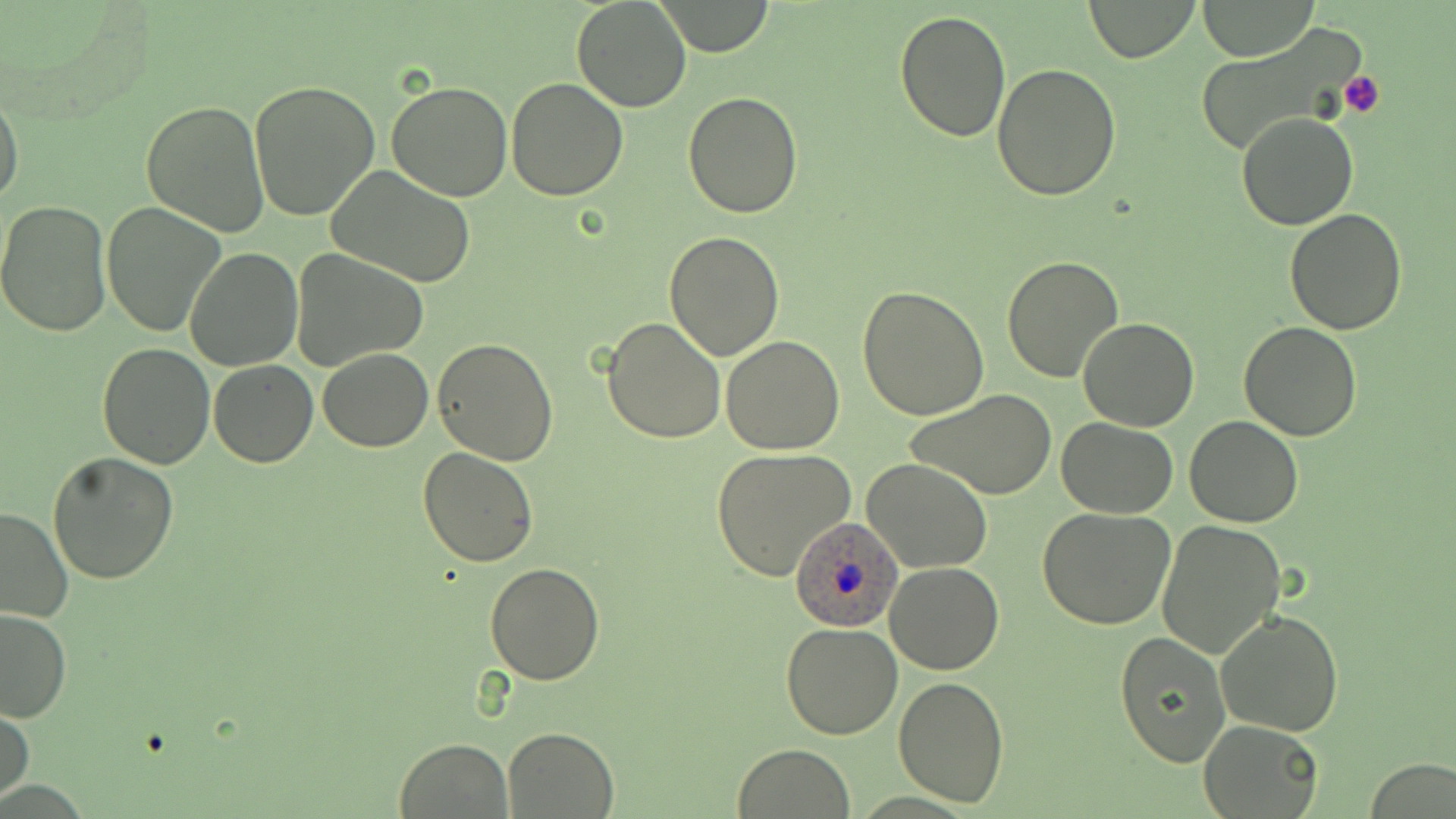
{
  "slide_level_diagnosis": "Plasmodium ovale",
  "stain": "May-Grünwald-Giemsa",
  "image_size": "1456×819 pixels",
  "modality": "optical microscopy",
  "preparation": "thin blood film",
  "plasmodium_ovale_infected_red_blood_cell_locations": "approximate bounding boxes as named x1/y1/x2/y2 corners in pixels: (x1=787, y1=513, x2=906, y2=632)",
  "magnification": "1000x",
  "field_of_view": "one of a larger specimen",
  "uninfected_red_blood_cell_locations": "approximate bounding boxes as named x1/y1/x2/y2 corners in pixels: (x1=571, y1=0, x2=691, y2=112), (x1=1082, y1=0, x2=1201, y2=63), (x1=1198, y1=0, x2=1320, y2=60), (x1=652, y1=1, x2=776, y2=55), (x1=894, y1=8, x2=1011, y2=142), (x1=1186, y1=25, x2=1377, y2=159), (x1=991, y1=62, x2=1122, y2=201), (x1=506, y1=77, x2=630, y2=201), (x1=248, y1=80, x2=380, y2=222), (x1=386, y1=81, x2=514, y2=201), (x1=1, y1=90, x2=25, y2=210), (x1=683, y1=92, x2=803, y2=218), (x1=142, y1=100, x2=269, y2=235), (x1=1236, y1=111, x2=1358, y2=230), (x1=326, y1=165, x2=477, y2=287), (x1=0, y1=199, x2=114, y2=337), (x1=102, y1=201, x2=227, y2=337), (x1=1283, y1=208, x2=1406, y2=334), (x1=663, y1=231, x2=783, y2=361), (x1=185, y1=248, x2=303, y2=370), (x1=292, y1=251, x2=427, y2=369), (x1=1002, y1=255, x2=1125, y2=384), (x1=859, y1=283, x2=990, y2=421), (x1=603, y1=317, x2=727, y2=443), (x1=1078, y1=318, x2=1200, y2=432), (x1=1239, y1=321, x2=1363, y2=441), (x1=721, y1=336, x2=846, y2=455), (x1=432, y1=337, x2=560, y2=464), (x1=97, y1=341, x2=216, y2=468), (x1=318, y1=347, x2=432, y2=451), (x1=208, y1=361, x2=318, y2=468), (x1=905, y1=388, x2=1056, y2=501), (x1=1185, y1=416, x2=1303, y2=528), (x1=1058, y1=419, x2=1179, y2=518), (x1=418, y1=447, x2=539, y2=565), (x1=710, y1=448, x2=857, y2=581), (x1=47, y1=451, x2=180, y2=585), (x1=862, y1=457, x2=993, y2=573), (x1=0, y1=506, x2=74, y2=624), (x1=1036, y1=507, x2=1177, y2=630), (x1=1156, y1=519, x2=1286, y2=659), (x1=482, y1=563, x2=606, y2=684), (x1=883, y1=563, x2=1004, y2=675), (x1=0, y1=609, x2=71, y2=724), (x1=1215, y1=610, x2=1345, y2=737), (x1=781, y1=621, x2=902, y2=739), (x1=1115, y1=630, x2=1231, y2=769), (x1=893, y1=677, x2=1009, y2=807), (x1=1, y1=705, x2=34, y2=803), (x1=1198, y1=719, x2=1324, y2=818), (x1=503, y1=727, x2=618, y2=817), (x1=395, y1=737, x2=511, y2=818), (x1=733, y1=742, x2=856, y2=818), (x1=1365, y1=759, x2=1452, y2=817)",
  "platelet_locations": "approximate bounding boxes as named x1/y1/x2/y2 corners in pixels: (x1=1338, y1=71, x2=1384, y2=118)"
}